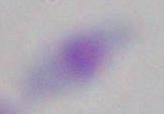
Summary:
  - Identification: Toxoplasma gondii
  - Modality: photomicrograph
  - Magnification: 1000x